Name the parasite shown.
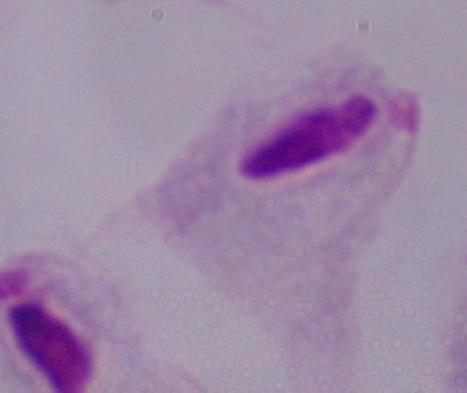
This is a trichomonad.

Micrograph. 1000x magnification.